Report the malaria status of this cell.
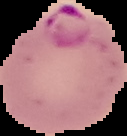

Parasitized.

Summary:
  - Image type: segmented cell region on a black background
  - Image size: 127×136 pixels
  - Preparation: thin blood smear